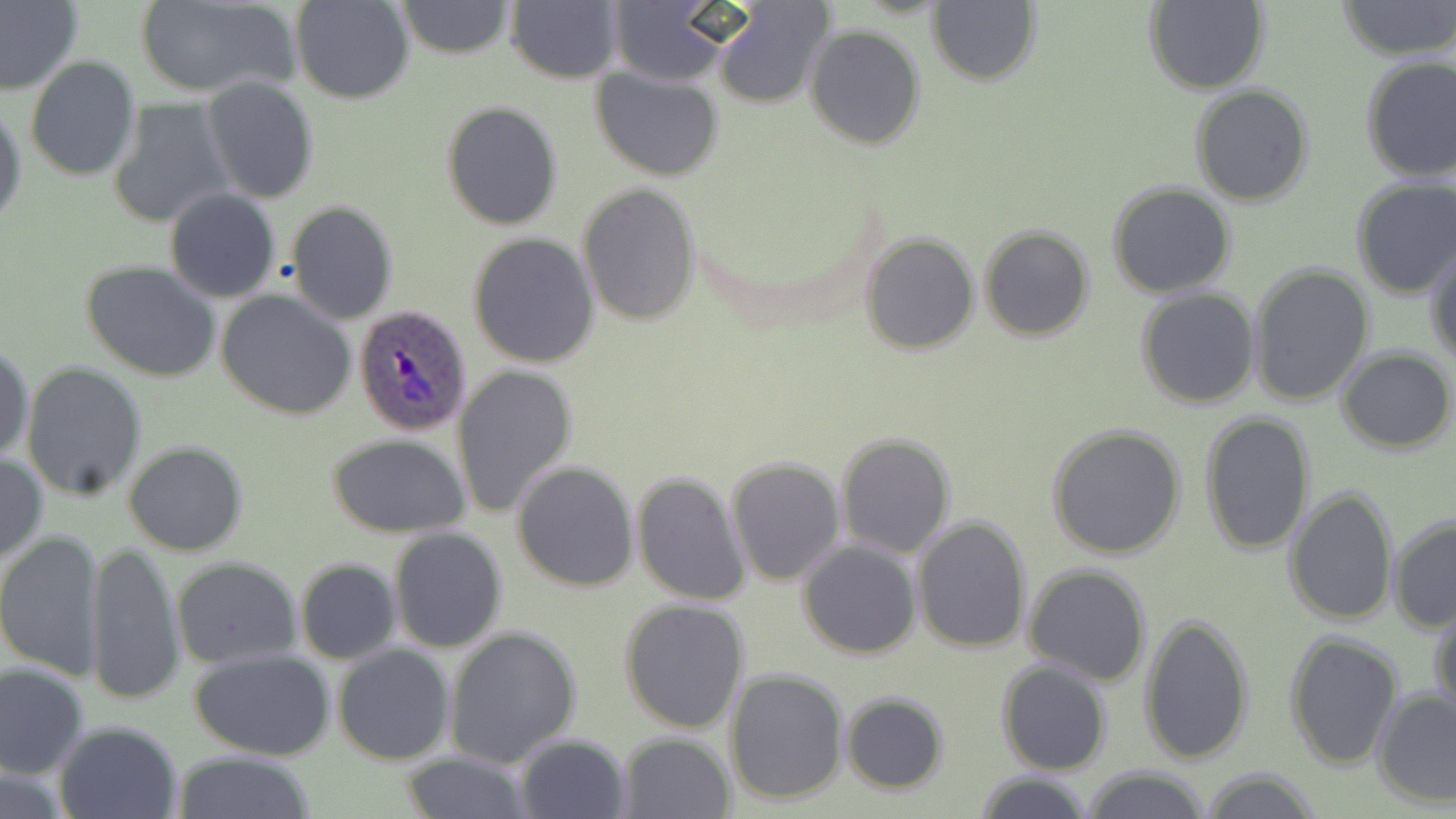
Summary:
  - Coordinate format: approximate bounding boxes as (x1, y1, x2, y2) in pixels
  - Uninfected red blood cell locations: (0, 0, 84, 97), (291, 0, 415, 104), (398, 0, 513, 59), (1336, 0, 1455, 60), (133, 1, 299, 98), (926, 1, 1041, 87), (1143, 1, 1269, 94), (505, 2, 623, 84), (604, 4, 734, 86), (712, 4, 833, 108), (805, 24, 925, 149), (1359, 54, 1456, 182), (24, 56, 141, 183), (590, 67, 726, 182), (202, 76, 319, 205), (1191, 84, 1314, 207), (1, 99, 25, 231), (110, 100, 233, 229), (441, 101, 563, 230), (1350, 177, 1456, 300), (1117, 180, 1248, 410), (578, 183, 703, 326), (1107, 183, 1237, 297), (164, 189, 282, 302), (287, 201, 398, 324), (979, 225, 1095, 342), (861, 232, 979, 353), (467, 233, 599, 368), (1426, 245, 1456, 367), (79, 261, 223, 385), (1247, 263, 1374, 407), (1135, 289, 1259, 410), (217, 291, 356, 420), (0, 339, 35, 465), (1337, 347, 1454, 454), (20, 363, 148, 501), (453, 363, 579, 517), (1198, 411, 1317, 555), (1045, 423, 1189, 560), (834, 432, 958, 559), (324, 433, 471, 537), (122, 440, 248, 555), (0, 451, 47, 565), (726, 456, 846, 585), (511, 461, 640, 591), (631, 471, 751, 607), (1284, 487, 1397, 627), (911, 515, 1033, 655), (1387, 515, 1456, 633), (387, 527, 509, 653), (0, 530, 105, 680), (86, 538, 184, 707), (798, 539, 922, 659), (172, 558, 301, 669), (294, 558, 401, 665), (1024, 563, 1151, 685), (619, 599, 750, 734), (1431, 602, 1455, 722), (1138, 613, 1255, 767), (443, 625, 582, 767), (1284, 631, 1402, 769), (333, 645, 455, 766), (187, 647, 340, 762), (996, 661, 1112, 775), (0, 663, 90, 780), (726, 669, 849, 805), (1372, 688, 1456, 808), (840, 692, 950, 794), (53, 721, 185, 819), (616, 732, 734, 817), (513, 734, 632, 819), (173, 753, 319, 818), (397, 754, 535, 817), (0, 762, 74, 817), (1081, 766, 1211, 819), (1198, 768, 1322, 819), (974, 772, 1097, 819)
  - Plasmodium ovale-infected red blood cell locations: (354, 305, 473, 434)
  - Slide-level diagnosis: Plasmodium ovale
  - Preparation: thin blood smear
  - Image size: 1456×819 pixels
  - Stain: May-Grünwald-Giemsa
  - Magnification: 1000x
  - Field of view: one of a larger specimen
  - Modality: optical microscopy